Outline each blood parasite and name the species.
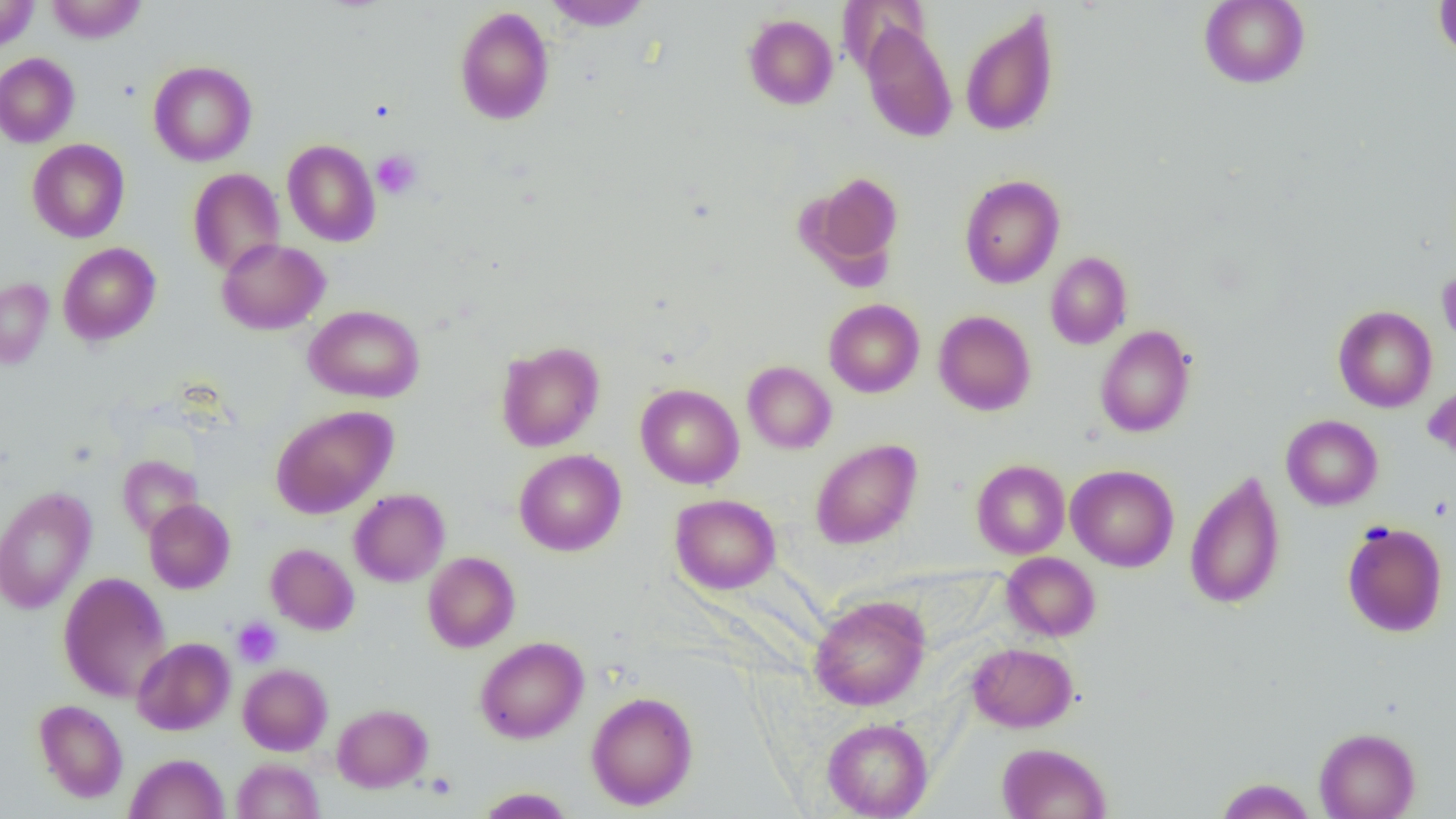
No blood parasites seen.

Approximate bounding boxes as (x1,y1)-(x2,y2) corner pairs in pixels. Uninfected red blood cell locations: (0,0)-(40,53), (46,0)-(146,42), (545,0)-(652,31), (1199,0)-(1310,88), (1434,0)-(1456,60), (455,6)-(554,125), (959,10)-(1059,137), (743,14)-(839,109), (859,21)-(958,142), (0,53)-(79,147), (148,61)-(257,166), (27,139)-(129,243), (283,140)-(380,247), (188,168)-(285,275), (804,171)-(904,281), (959,175)-(1064,288), (216,238)-(329,335), (58,242)-(160,345), (1045,252)-(1132,349), (1438,264)-(1456,354), (0,278)-(53,368), (824,299)-(924,397), (305,305)-(424,403), (1333,306)-(1437,412), (933,310)-(1036,415), (1095,325)-(1195,437), (496,341)-(605,452), (743,361)-(836,453), (1423,378)-(1456,467), (635,384)-(744,489), (271,405)-(397,518), (1281,414)-(1382,510), (810,439)-(922,549), (514,449)-(626,556), (118,455)-(201,539), (971,459)-(1070,559), (1066,465)-(1179,572), (1185,472)-(1286,609), (0,487)-(97,615), (349,489)-(450,586), (670,494)-(780,594), (144,499)-(235,593), (1341,520)-(1448,637), (265,543)-(359,634), (423,551)-(519,652), (1002,552)-(1100,641), (58,572)-(171,702), (809,594)-(930,711), (475,636)-(588,743), (132,637)-(235,735), (968,643)-(1078,732), (238,663)-(332,755), (586,691)-(697,810), (34,699)-(128,802), (332,704)-(432,792), (822,718)-(933,818), (1314,727)-(1420,819), (997,742)-(1111,818), (125,753)-(229,819), (232,758)-(324,819), (1215,777)-(1316,819), (476,787)-(575,818). Platelet locations: (371,150)-(422,199), (232,618)-(282,668). Slide-level diagnosis: negative for blood parasites. 1000x magnification. One field of a larger specimen. Optical microscopy. Image is 1456×819 pixels. Thin blood film.